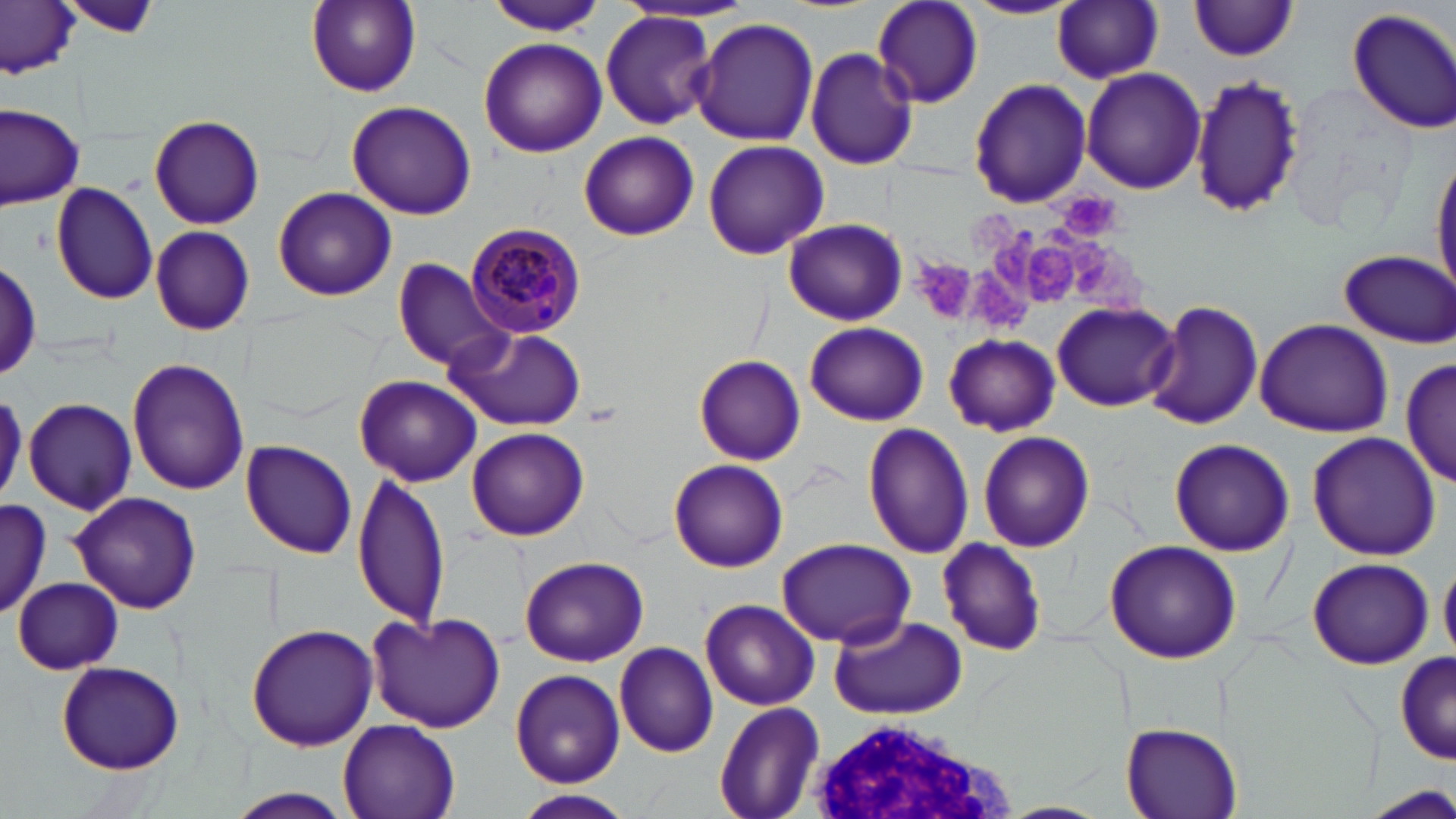
Summary:
  - Coordinate format: approximate bounding boxes as (x1, y1, x2, y2) in pixels
  - Uninfected red blood cell locations: (65, 0, 164, 40), (871, 0, 983, 108), (306, 1, 422, 96), (484, 1, 608, 34), (961, 1, 1082, 20), (1051, 1, 1165, 84), (1188, 1, 1302, 61), (0, 2, 81, 77), (1346, 6, 1456, 136), (600, 13, 719, 129), (690, 17, 818, 145), (477, 36, 607, 157), (805, 47, 918, 170), (1080, 66, 1204, 193), (1190, 73, 1305, 219), (968, 78, 1092, 209), (344, 100, 478, 220), (1, 105, 85, 210), (148, 113, 264, 230), (579, 131, 700, 240), (702, 139, 828, 261), (1431, 146, 1456, 300), (50, 180, 158, 305), (273, 185, 397, 301), (783, 217, 907, 327), (150, 226, 256, 337), (1338, 249, 1456, 346), (1, 256, 41, 383), (391, 258, 514, 373), (1143, 299, 1264, 433), (1052, 300, 1181, 410), (1253, 319, 1393, 437), (804, 322, 928, 425), (447, 326, 587, 432), (943, 333, 1061, 436), (1399, 353, 1454, 489), (695, 356, 806, 466), (126, 358, 250, 494), (354, 374, 481, 486), (23, 398, 138, 514), (863, 424, 974, 559), (467, 427, 589, 541), (977, 430, 1094, 552), (1307, 431, 1440, 560), (1169, 437, 1295, 557), (241, 439, 358, 560), (669, 459, 788, 572), (350, 469, 450, 631), (67, 492, 202, 614), (0, 497, 50, 621), (776, 538, 917, 648), (937, 539, 1047, 656), (1104, 540, 1241, 665), (520, 555, 649, 667), (1307, 558, 1434, 669), (1439, 561, 1456, 663), (13, 576, 122, 674), (702, 598, 819, 710), (365, 610, 507, 734), (829, 613, 965, 719), (245, 622, 378, 753), (614, 641, 718, 758), (1394, 651, 1454, 765), (55, 660, 185, 774), (511, 669, 626, 789), (713, 701, 826, 819), (337, 720, 459, 819), (1122, 722, 1243, 819), (220, 789, 357, 819), (519, 790, 633, 818), (996, 800, 1109, 819)
  - Plasmodium malariae-infected red blood cell locations: (466, 222, 588, 339)
  - Platelet locations: (1056, 189, 1123, 238), (986, 224, 1038, 290), (1077, 240, 1124, 298), (1031, 245, 1078, 300), (916, 253, 973, 320), (975, 270, 1029, 329)
  - White blood cell locations: (794, 721, 1020, 819)
  - Slide-level diagnosis: Plasmodium malariae
  - Field of view: single
  - Image size: 1456×819 pixels
  - Magnification: 1000x
  - Modality: light microscopy
  - Stain: May-Grünwald-Giemsa
  - Preparation: thin blood smear